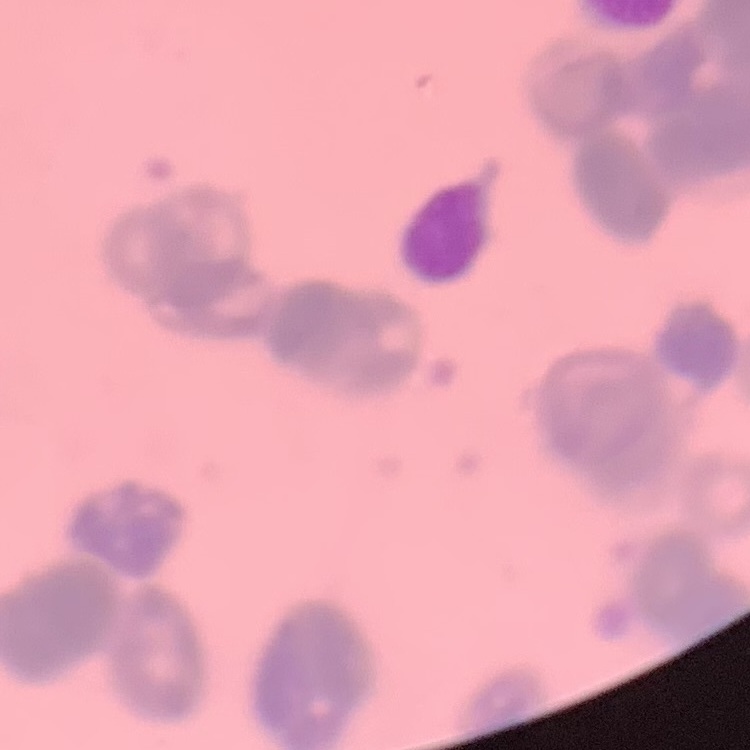

The red blood cells exhibit rouleaux formation. Thin blood smear. One tile cut from a larger photomicrograph. Field's or Giemsa stain.